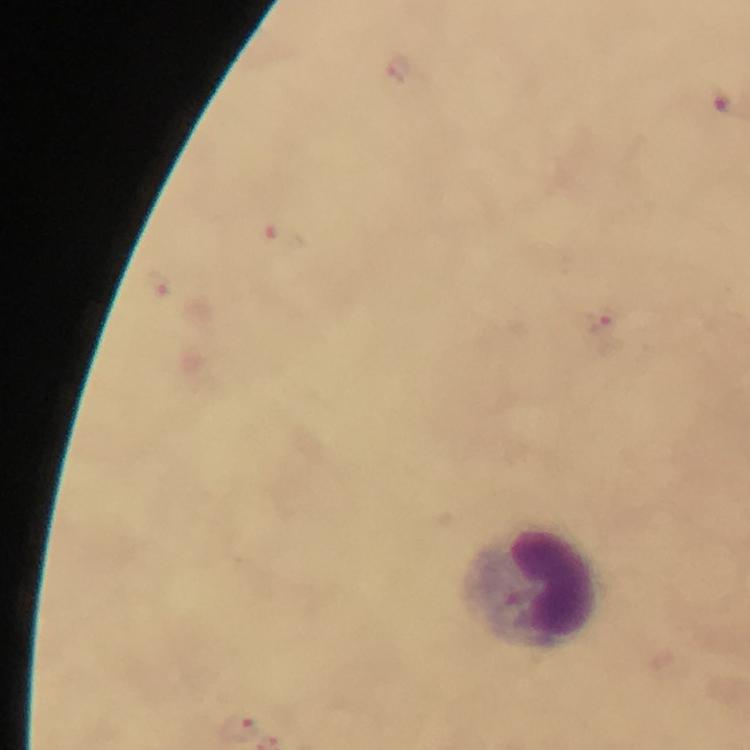
image size = 750×750 pixels
stain = Giemsa
immersion oil = applied
magnification = 100x
context = from a diagnostic examination for malaria
leukocyte locations = approximate centers as [x, y] in pixels: [539, 589]
preparation = thick smear
cropped from = one field of view
capture = smartphone camera through the microscope
Plasmodium parasite locations = approximate centers as [x, y] in pixels: [281, 241], [158, 285], [607, 324], [238, 725]